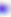

Photomicrograph. Toxoplasma gondii is shown. 400x magnification.